Locate every Babesia divergens-infected red blood cell.
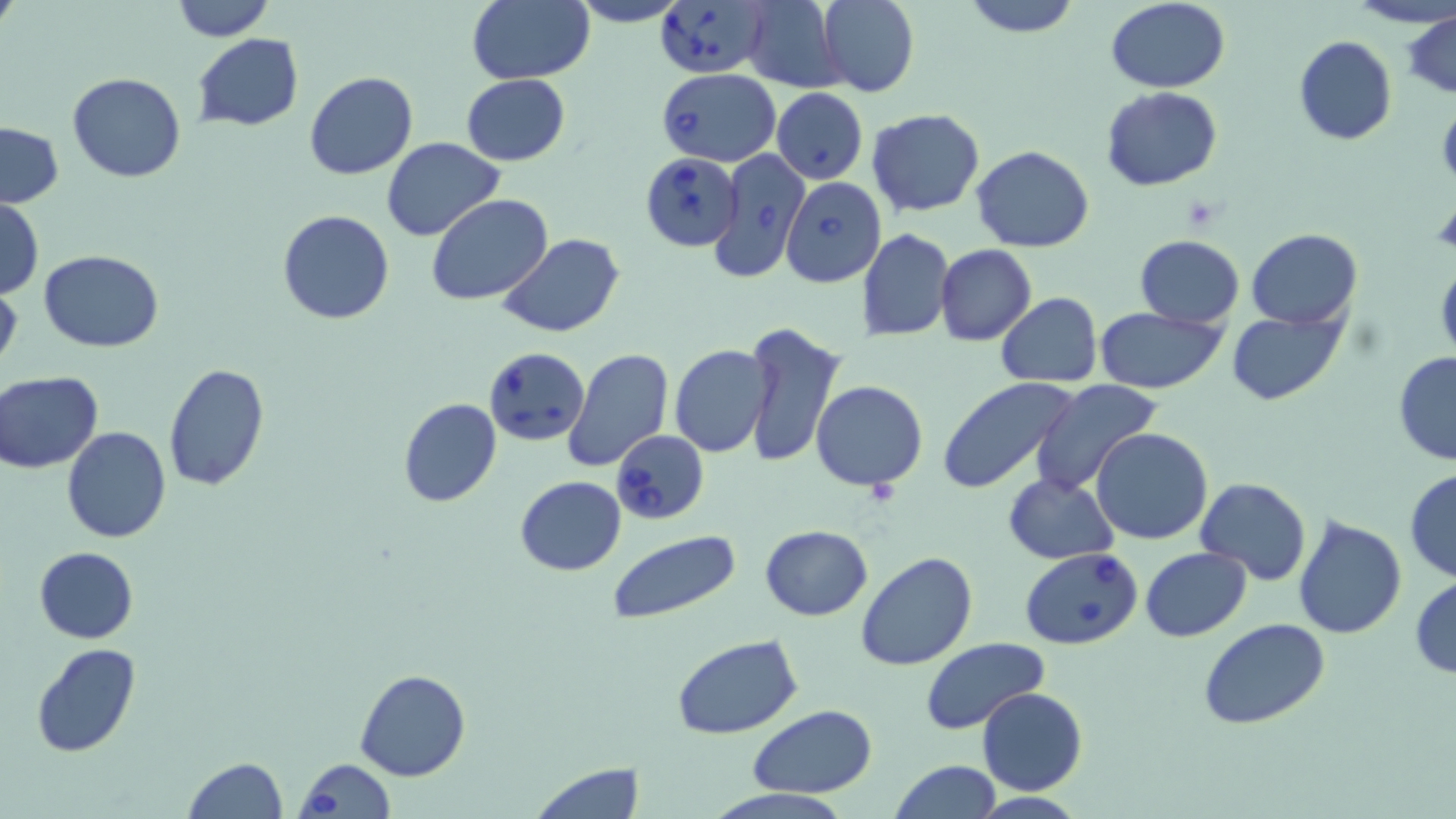
Approximate bounding boxes as [x1, y1, x2, y2] in pixels.
Babesia divergens-infected red blood cells: [653, 0, 772, 77], [657, 67, 781, 165], [707, 148, 812, 283], [640, 151, 743, 253], [780, 177, 886, 287], [483, 346, 590, 447], [610, 430, 709, 524], [1019, 547, 1143, 649], [294, 757, 395, 819].

Summary:
  - Uninfected red blood cell locations: [172, 0, 275, 41], [566, 0, 693, 27], [740, 0, 848, 92], [816, 0, 919, 97], [961, 0, 1081, 37], [1105, 0, 1230, 92], [1344, 0, 1456, 29], [466, 1, 595, 84], [1403, 9, 1456, 99], [193, 34, 303, 131], [1293, 35, 1397, 146], [304, 70, 417, 180], [67, 72, 187, 182], [462, 74, 570, 166], [771, 87, 868, 184], [1100, 87, 1223, 192], [866, 108, 986, 218], [0, 122, 63, 208], [381, 138, 505, 240], [971, 144, 1093, 253], [426, 195, 552, 306], [0, 196, 43, 299], [278, 211, 396, 325], [858, 228, 953, 342], [1246, 228, 1362, 328], [498, 234, 624, 338], [1135, 234, 1244, 328], [937, 245, 1036, 346], [39, 250, 164, 351], [1436, 262, 1456, 366], [0, 280, 22, 377], [995, 294, 1103, 386], [1095, 307, 1227, 393], [1227, 308, 1347, 405], [742, 321, 846, 469], [669, 344, 772, 457], [562, 347, 674, 472], [1392, 351, 1456, 467], [162, 363, 270, 492], [0, 371, 103, 474], [937, 376, 1080, 496], [1028, 378, 1164, 496], [812, 380, 927, 492], [397, 398, 502, 507], [62, 428, 171, 545], [1092, 428, 1213, 546], [1405, 468, 1456, 583], [1004, 473, 1118, 564], [514, 476, 627, 575], [1194, 477, 1311, 586], [1293, 513, 1407, 640], [760, 524, 873, 621], [609, 532, 739, 624], [34, 546, 139, 644], [1141, 548, 1252, 641], [856, 552, 978, 672], [1411, 575, 1456, 677], [1198, 617, 1330, 730], [672, 635, 804, 741], [921, 638, 1048, 735], [29, 643, 141, 759], [355, 669, 471, 782], [976, 686, 1088, 796], [748, 706, 879, 796], [182, 757, 287, 819], [889, 760, 1001, 818], [530, 763, 644, 818]
  - Slide-level diagnosis: Babesia divergens
  - Preparation: thin blood film
  - Image size: 1456×819 pixels
  - Modality: optical microscopy
  - Stain: May-Grünwald-Giemsa
  - Field of view: one of a larger specimen
  - Magnification: 1000x